Classify this cell by malaria status.
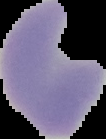
It is parasitized.

Image is 106×139 pixels. The area outside the segmented cell region is set to black. From a thin blood film.